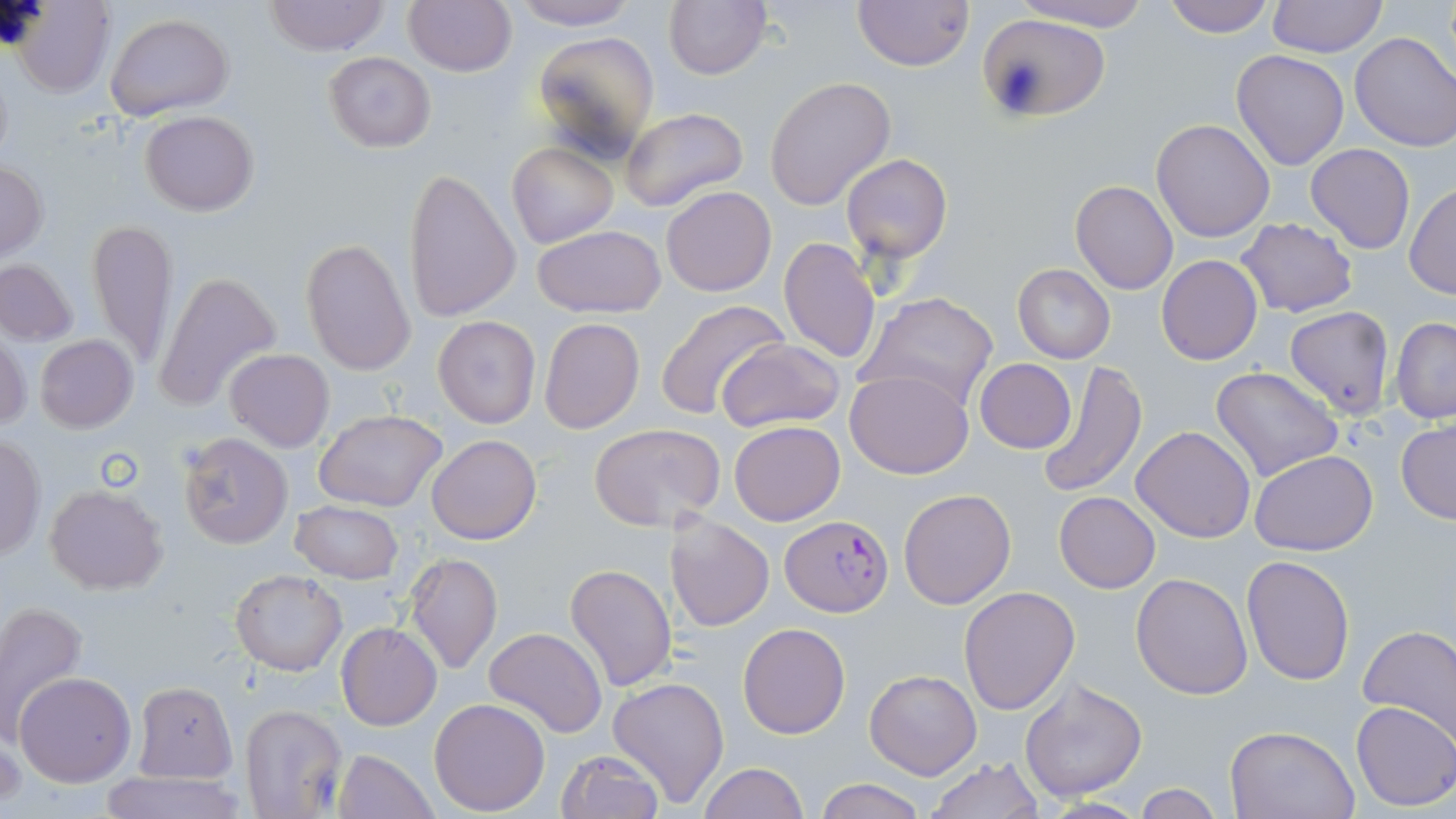

{
  "slide_level_diagnosis": "Plasmodium falciparum",
  "modality": "optical microscopy",
  "stain": "May-Grünwald-Giemsa",
  "magnification": "1000x",
  "uninfected_red_blood_cell_locations": "approximate bounding boxes as (x1,y1)-(x2,y2) corner pairs in pixels: (402,0)-(517,75), (512,0)-(637,28), (662,0)-(773,81), (852,0)-(974,71), (1012,0)-(1154,31), (1163,0)-(1274,38), (11,1)-(115,95), (263,1)-(390,55), (1266,1)-(1388,56), (105,13)-(234,119), (975,13)-(1110,124), (530,30)-(660,161), (1349,31)-(1456,151), (1237,41)-(1449,155), (1230,50)-(1349,171), (324,51)-(436,153), (765,77)-(896,212), (620,106)-(749,213), (140,110)-(257,216), (1150,118)-(1274,242), (508,141)-(617,248), (1305,143)-(1415,254), (842,154)-(951,262), (0,162)-(48,261), (404,168)-(522,321), (1070,180)-(1178,294), (1405,183)-(1455,298), (661,186)-(778,296), (87,216)-(179,370), (1236,217)-(1358,317), (534,225)-(666,317), (779,237)-(880,365), (300,239)-(415,376), (1156,254)-(1262,366), (0,258)-(79,346), (1012,263)-(1115,363), (154,269)-(282,414), (855,290)-(1000,413), (654,300)-(791,424), (1284,306)-(1395,419), (433,316)-(539,428), (1390,316)-(1456,423), (539,317)-(646,435), (0,329)-(31,433), (35,335)-(139,434), (717,338)-(845,434), (224,348)-(334,451), (974,358)-(1074,453), (1034,362)-(1148,496), (1211,365)-(1343,483), (844,369)-(974,479), (314,409)-(447,512), (729,421)-(846,527), (588,422)-(725,531), (1396,422)-(1456,524), (1132,426)-(1256,544), (177,433)-(292,549), (426,433)-(541,545), (1,435)-(45,559), (1249,449)-(1378,557), (45,485)-(168,595), (898,489)-(1015,608), (1054,491)-(1160,592), (291,498)-(402,584), (665,513)-(775,630), (405,552)-(503,674), (1241,554)-(1356,686), (565,564)-(676,693), (229,569)-(346,676), (1132,572)-(1255,699), (958,585)-(1081,715), (0,602)-(87,742), (337,622)-(441,731), (738,622)-(851,739), (1358,624)-(1456,746), (484,626)-(607,738), (864,669)-(981,779), (14,672)-(135,787), (608,675)-(728,806), (1018,676)-(1148,803), (134,682)-(236,783), (430,698)-(551,816), (1351,701)-(1456,812), (238,703)-(348,819), (1,724)-(24,811), (1225,725)-(1359,819), (333,748)-(438,819), (556,749)-(664,819), (925,757)-(1043,818), (697,762)-(808,819), (97,766)-(246,819), (814,778)-(927,819), (1131,782)-(1225,818), (1037,798)-(1150,818)",
  "image_size": "1456×819 pixels",
  "field_of_view": "single",
  "plasmodium_falciparum_infected_red_blood_cell_locations": "approximate bounding boxes as (x1,y1)-(x2,y2) corner pairs in pixels: (780,514)-(893,617)",
  "preparation": "thin blood smear"
}